Report the malaria status of this cell.
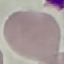
It is uninfected.

stain = Giemsa
preparation = thin blood film
capture = smartphone through the microscope eyepiece
image type = automatically extracted cell patch, resized to 64 × 64 pixels